State which parasite is depicted.
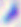

This is Toxoplasma gondii.

Summary:
  - Magnification: 400x
  - Modality: micrograph